Name the parasite shown.
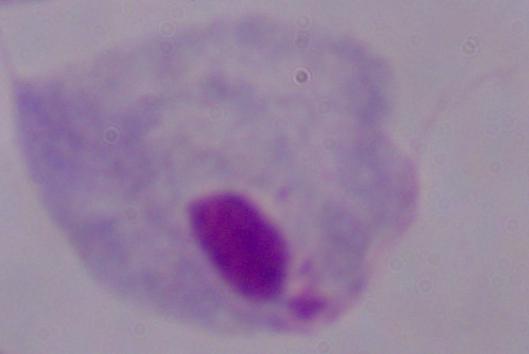

This is a trichomonad.

Summary:
  - Modality: photomicrograph
  - Magnification: 1000x